Point out every malaria parasite.
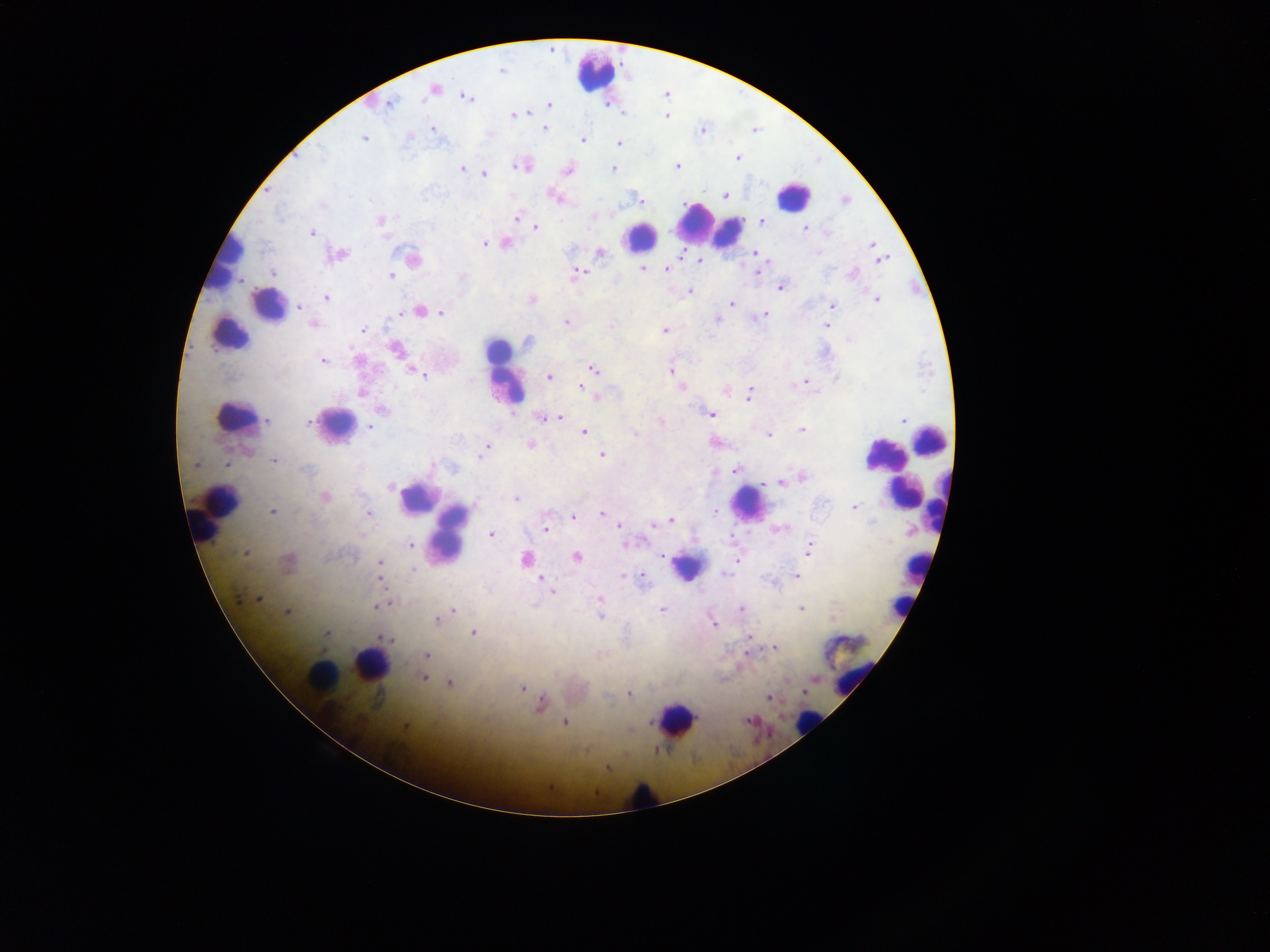
Approximate centers as x y in pixels.
Malaria parasites: 501 70; 434 89; 467 97; 389 103; 550 105; 528 113; 513 115; 666 116; 544 128; 433 129; 702 130; 364 139; 583 140; 618 144; 321 156; 738 158; 677 166; 521 167; 462 169; 613 169; 567 171; 484 175; 726 195; 556 197; 638 198; 845 200; 322 207; 593 216; 517 217; 380 220; 761 221; 537 228; 806 228; 826 232; 311 233; 485 243; 506 243; 872 245; 600 253; 756 253; 818 253; 338 254; 413 259; 881 259; 700 261; 642 269; 666 269; 757 271; 578 273; 273 274; 391 275; 852 275; 463 276; 781 286; 690 291; 326 298; 532 300; 877 300; 732 302; 833 305; 300 307; 419 311; 441 312; 763 315; 757 317; 716 319; 566 322; 314 324; 611 325; 827 325; 363 330; 665 330; 849 339; 528 342; 397 349; 358 361; 323 362; 593 369; 671 371; 422 375; 549 376; 806 382; 581 387; 682 388; 725 391; 362 393; 749 394; 383 411; 711 414; 560 417; 542 418; 309 420; 903 420; 268 421; 660 421; 370 426; 803 430; 584 432; 635 434; 768 434; 530 445; 485 449; 483 453; 602 455; 274 460; 196 464; 226 464; 735 469; 307 470; 802 478; 781 483; 390 486; 325 497; 516 499; 854 507; 274 511; 715 511; 369 513; 602 514; 573 517; 670 520; 654 524; 619 525; 545 528; 491 534; 410 544; 810 549; 245 553; 662 555; 576 556; 526 559; 288 560; 380 563; 413 570; 623 576; 796 576; 381 579; 642 579; 541 580; 546 584; 552 592; 240 598; 258 600; 600 600; 380 605; 801 608; 662 609; 741 609; 287 612; 452 612; 600 617; 438 620; 713 623; 473 633; 327 634; 749 636; 387 639; 774 648; 427 655; 423 678; 449 683; 522 688; 629 694; 768 697; 541 704; 748 721; 564 722; 630 730; 607 768.

Leukocyte locations: 597 75; 792 196; 698 224; 729 233; 641 236; 226 259; 269 306; 229 333; 505 372; 233 416; 336 424; 929 437; 884 454; 899 491; 416 498; 747 504; 937 504; 218 513; 450 533; 687 567; 914 567; 908 604; 371 665; 855 675; 321 676; 675 718; 808 722; 643 796. Sample from Ghana. Single field of view. Mobile-phone photograph taken through the microscope. Thick blood smear. Image is 1270×952 pixels.